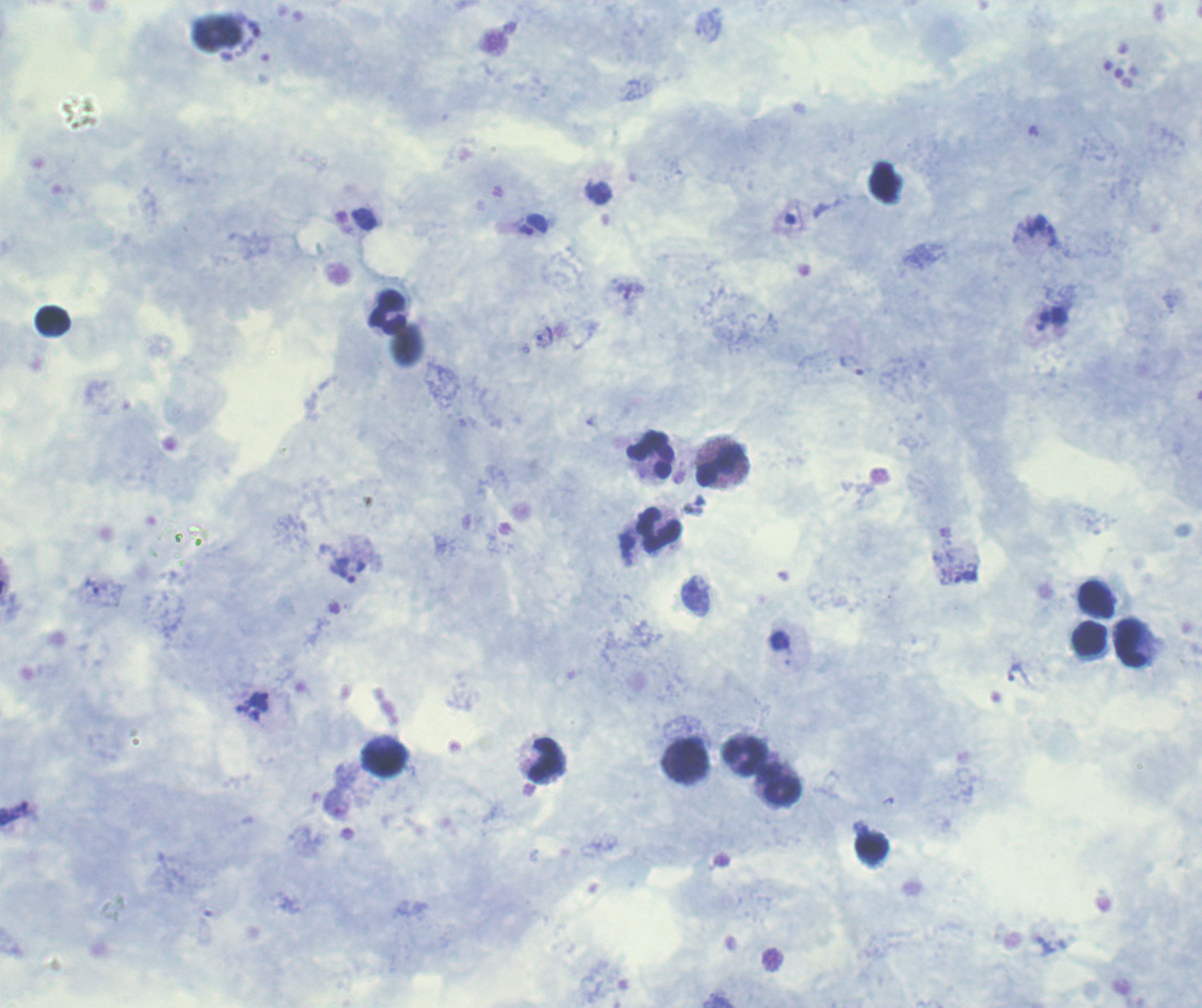

Approximate object centers, in pixels from the top-left corner.
Summary:
  - Trophozoite locations: (x=363, y=219), (x=536, y=225), (x=1046, y=229), (x=546, y=335), (x=967, y=578), (x=781, y=641), (x=260, y=700)
  - Leukocyte locations: (x=388, y=312), (x=54, y=321), (x=650, y=454), (x=720, y=465), (x=659, y=530), (x=1098, y=599), (x=1090, y=639), (x=1131, y=643), (x=746, y=757), (x=386, y=759), (x=547, y=759), (x=688, y=759), (x=783, y=790), (x=872, y=847)
  - Background quality: good
  - Context: previously used in an actual diagnosis
  - Image size: 1202×1008 pixels
  - Field of view: one from this slide
  - Magnification: 100x
  - Result: positive for Plasmodium parasites
  - Preparation: thick smear of blood
  - Coloration quality: good
  - Stain: Romanowsky